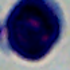

1000x magnification. Photomicrograph. A white blood cell is seen.